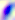
{
  "identification": "Toxoplasma gondii",
  "magnification": "400x",
  "modality": "photomicrograph"
}